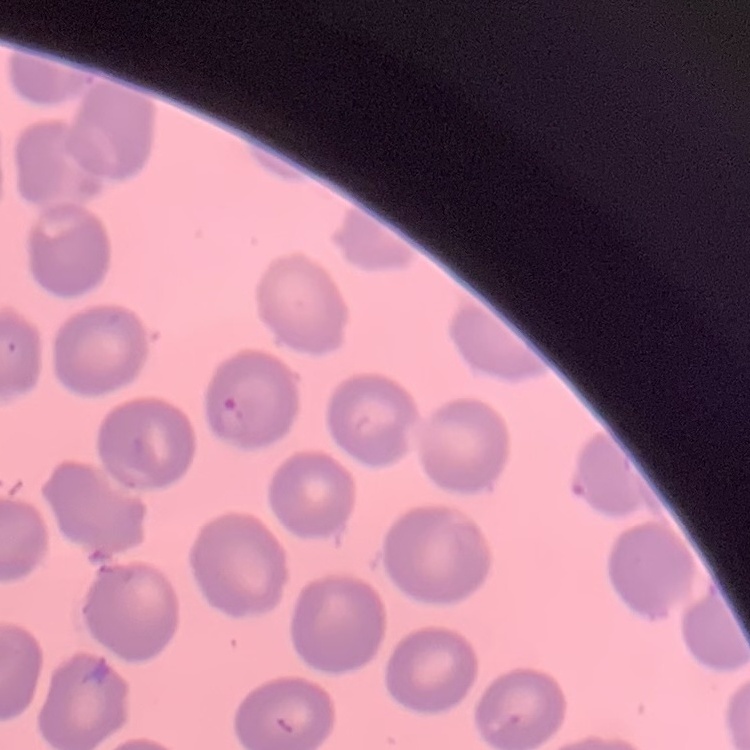

The erythrocytes exhibit no rouleaux formation. Field's or Giemsa stain. Thin blood smear. One tile cut from a larger photomicrograph.